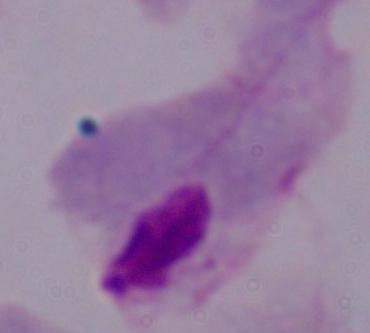

magnification: 1000x
identification: trichomonad
modality: photomicrograph